Point out every malaria parasite and every leukocyte.
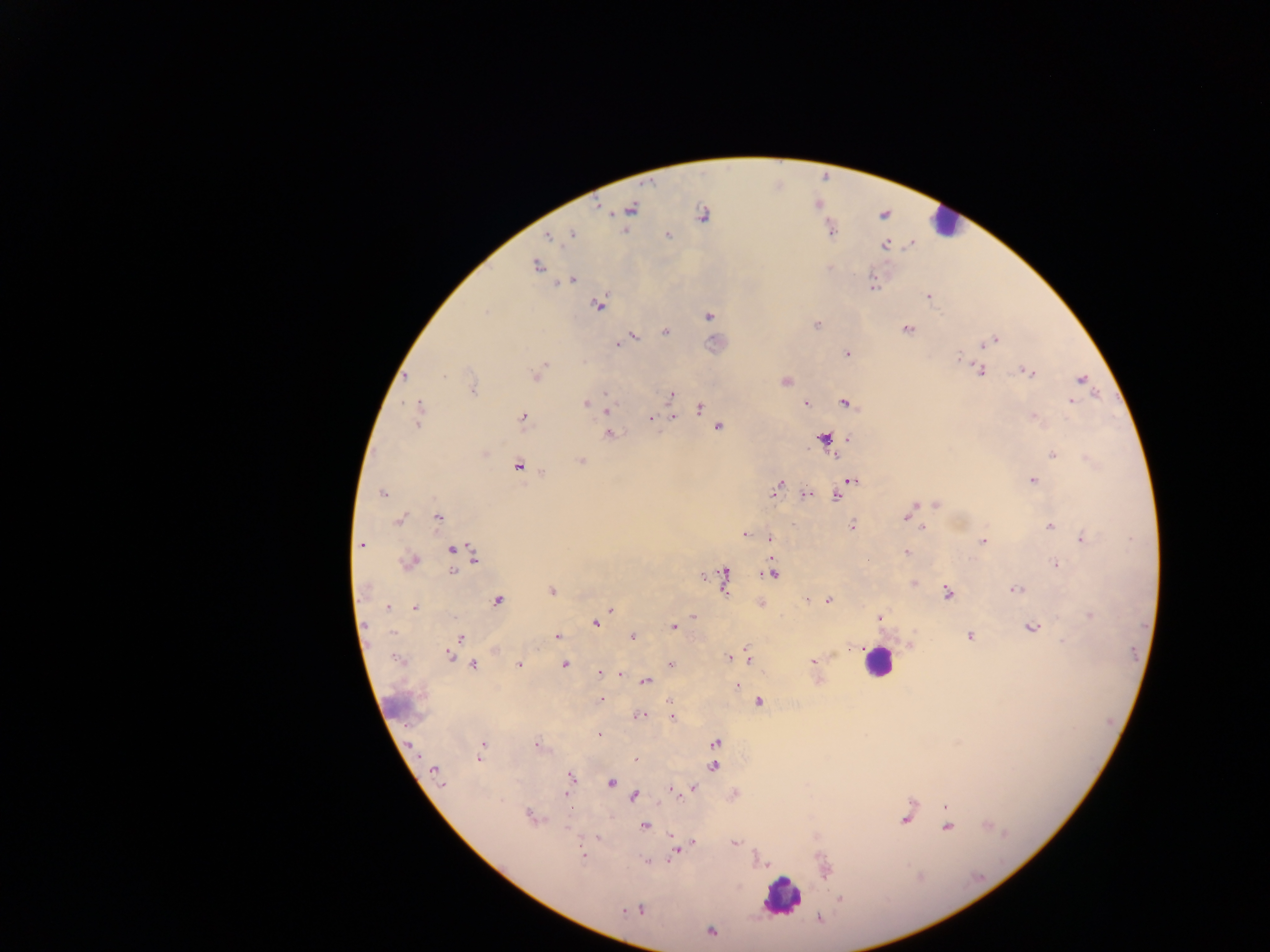
Approximate centers as x y in pixels.
Malaria parasites: 597 207; 631 210; 610 214; 703 215; 572 233; 668 235; 547 239; 536 266; 573 280; 598 305; 708 315; 817 325; 907 329; 665 332; 635 337; 997 338; 617 344; 847 354; 956 356; 544 363; 1024 369; 981 371; 1031 371; 539 372; 445 375; 534 376; 1081 378; 785 382; 472 388; 475 391; 604 393; 671 393; 805 402; 845 402; 1072 402; 584 403; 418 408; 700 408; 608 410; 521 416; 672 417; 1034 417; 652 418; 417 420; 718 426; 609 434; 823 438; 486 453; 1053 454; 582 461; 518 467; 1034 480; 851 481; 776 487; 382 492; 773 493; 840 493; 806 494; 836 497; 935 503; 922 504; 913 506; 909 516; 437 517; 905 518; 398 520; 853 525; 1050 526; 924 528; 742 535; 1081 535; 771 539; 982 541; 362 545; 451 550; 472 552; 907 552; 474 560; 414 562; 1054 564; 771 571; 453 572; 724 572; 703 577; 914 582; 726 585; 1014 590; 550 592; 946 592; 829 599; 498 600; 387 608; 416 608; 610 609; 1088 614; 693 615; 878 616; 367 624; 595 625; 1030 627; 673 628; 392 634; 970 636; 632 637; 462 638; 558 638; 1062 640; 850 648; 454 649; 745 649; 841 649; 495 652; 835 654; 450 655; 728 657; 751 662; 814 662; 671 663; 473 664; 519 664; 564 664; 597 673; 622 676; 818 678; 645 682; 737 686; 600 700; 670 701; 759 701; 639 716; 671 718; 599 735; 537 742; 716 742; 957 742; 411 745; 481 746; 480 757; 636 759; 714 767; 433 771; 569 776; 612 784; 442 785; 694 789; 671 791; 635 797; 569 803; 944 805; 528 816; 903 820; 645 827; 568 828; 946 829; 671 837; 598 838; 694 842; 736 843; 583 853; 673 854; 645 861; 839 899; 818 917; 709 930.
Leukocytes: 939 223; 879 664; 779 896.

country = Ghana
preparation = thick blood smear
capture = mobile-phone photograph through a microscope
field of view = single
image size = 1270×952 pixels